Give the position of every malaria parasite and every leukocyte.
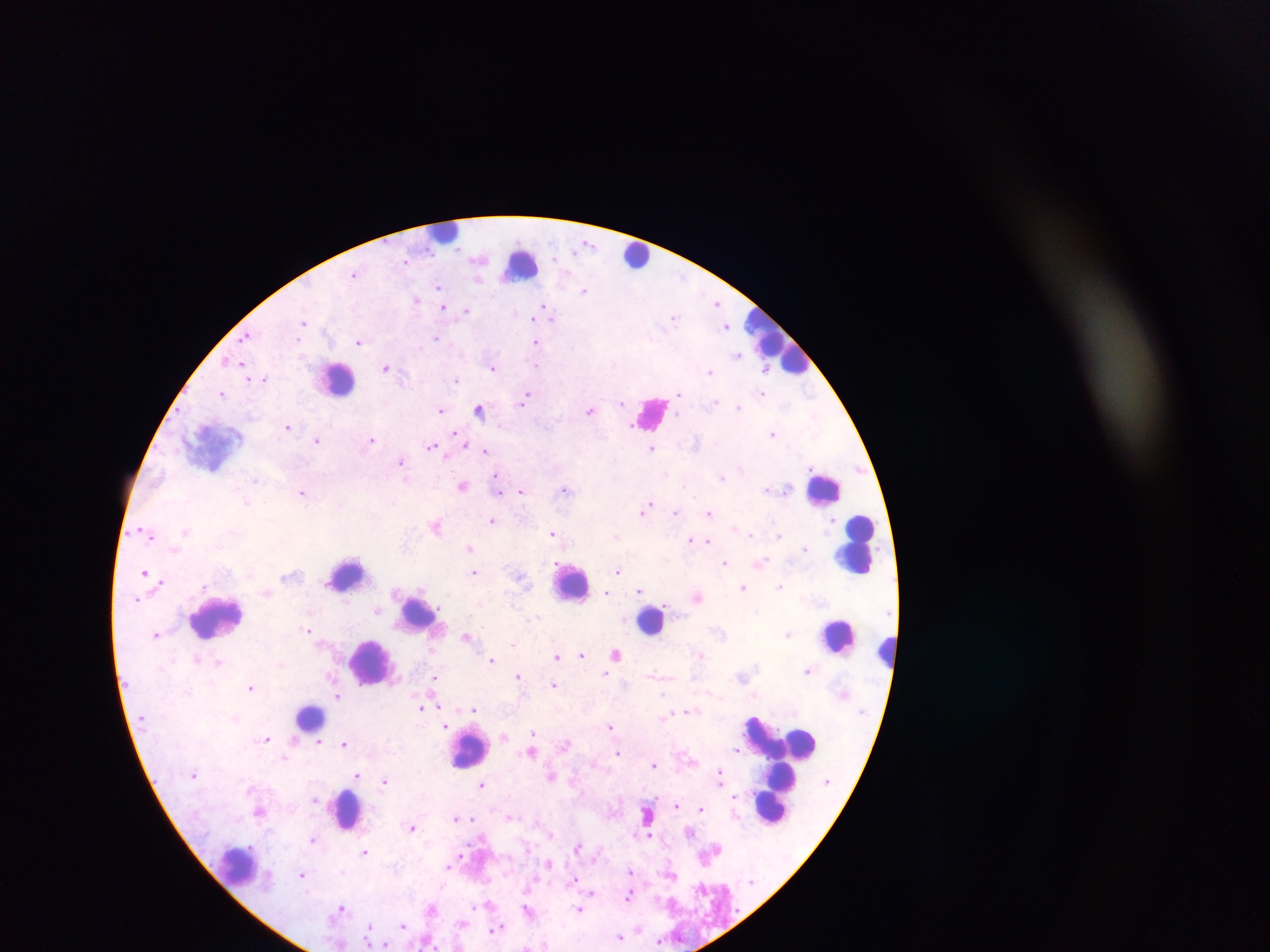

Approximate centers as [x, y] in pixels.
Malaria parasites: [587, 243], [355, 273], [439, 286], [584, 289], [417, 299], [718, 302], [544, 306], [443, 307], [466, 310], [533, 318], [674, 318], [304, 322], [727, 326], [246, 336], [436, 337], [360, 342], [536, 342], [739, 354], [538, 363], [386, 366], [494, 366], [765, 366], [710, 371], [265, 378], [456, 380], [222, 393], [762, 393], [679, 394], [527, 395], [623, 401], [741, 407], [441, 409], [480, 409], [591, 410], [289, 426], [773, 433], [371, 439], [317, 440], [464, 444], [432, 446], [652, 448], [486, 451], [401, 462], [499, 475], [723, 476], [463, 484], [498, 485], [767, 487], [521, 490], [566, 490], [498, 491], [303, 492], [247, 502], [646, 508], [676, 512], [710, 512], [493, 521], [833, 522], [436, 524], [144, 531], [187, 531], [553, 533], [616, 534], [750, 534], [780, 534], [691, 538], [708, 539], [471, 548], [805, 549], [725, 562], [761, 563], [618, 570], [146, 572], [475, 572], [780, 585], [744, 587], [642, 588], [607, 592], [640, 593], [698, 597], [377, 610], [308, 630], [156, 633], [788, 634], [466, 636], [513, 644], [702, 653], [581, 654], [616, 654], [558, 655], [196, 658], [492, 659], [218, 662], [808, 670], [606, 673], [519, 675], [435, 679], [555, 684], [251, 687], [338, 696], [441, 706], [421, 708], [474, 709], [690, 710], [236, 718], [610, 725], [447, 726], [533, 733], [503, 736], [267, 739], [567, 742], [319, 743], [344, 743], [736, 749], [531, 750], [618, 752], [285, 758], [655, 764], [357, 774], [552, 775], [720, 775], [386, 780], [482, 783], [314, 800], [677, 806], [701, 808], [260, 810], [648, 813], [511, 816], [456, 818], [473, 819], [413, 827], [690, 831], [551, 834], [647, 836], [312, 839], [577, 846], [366, 852], [461, 855], [550, 863], [449, 868], [631, 872], [672, 874], [303, 875], [574, 877], [592, 892], [628, 893], [489, 903], [342, 907], [432, 907], [529, 910], [580, 910], [463, 922], [402, 924], [370, 925], [497, 928], [638, 928], [621, 937], [660, 941], [369, 944], [383, 945], [527, 946], [458, 947].
Leukocytes: [445, 233], [636, 256], [521, 262], [778, 342], [338, 379], [651, 414], [824, 488], [857, 544], [347, 576], [571, 581], [417, 611], [216, 617], [651, 620], [838, 635], [885, 650], [372, 661], [309, 717], [768, 733], [793, 741], [801, 742], [469, 749], [783, 756], [781, 780], [777, 781], [773, 803], [347, 809], [240, 866].

Summary:
  - Capture: mobile-phone photograph through a microscope
  - Country: Ghana
  - Image size: 1270×952 pixels
  - Preparation: thick blood smear
  - Field of view: single